Assess this cell for malaria.
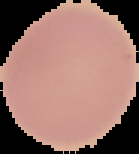
Uninfected.

Image is 139×154 pixels. From a thin blood film. Cell region segmented out of the field of view; the surrounding area is masked to black.